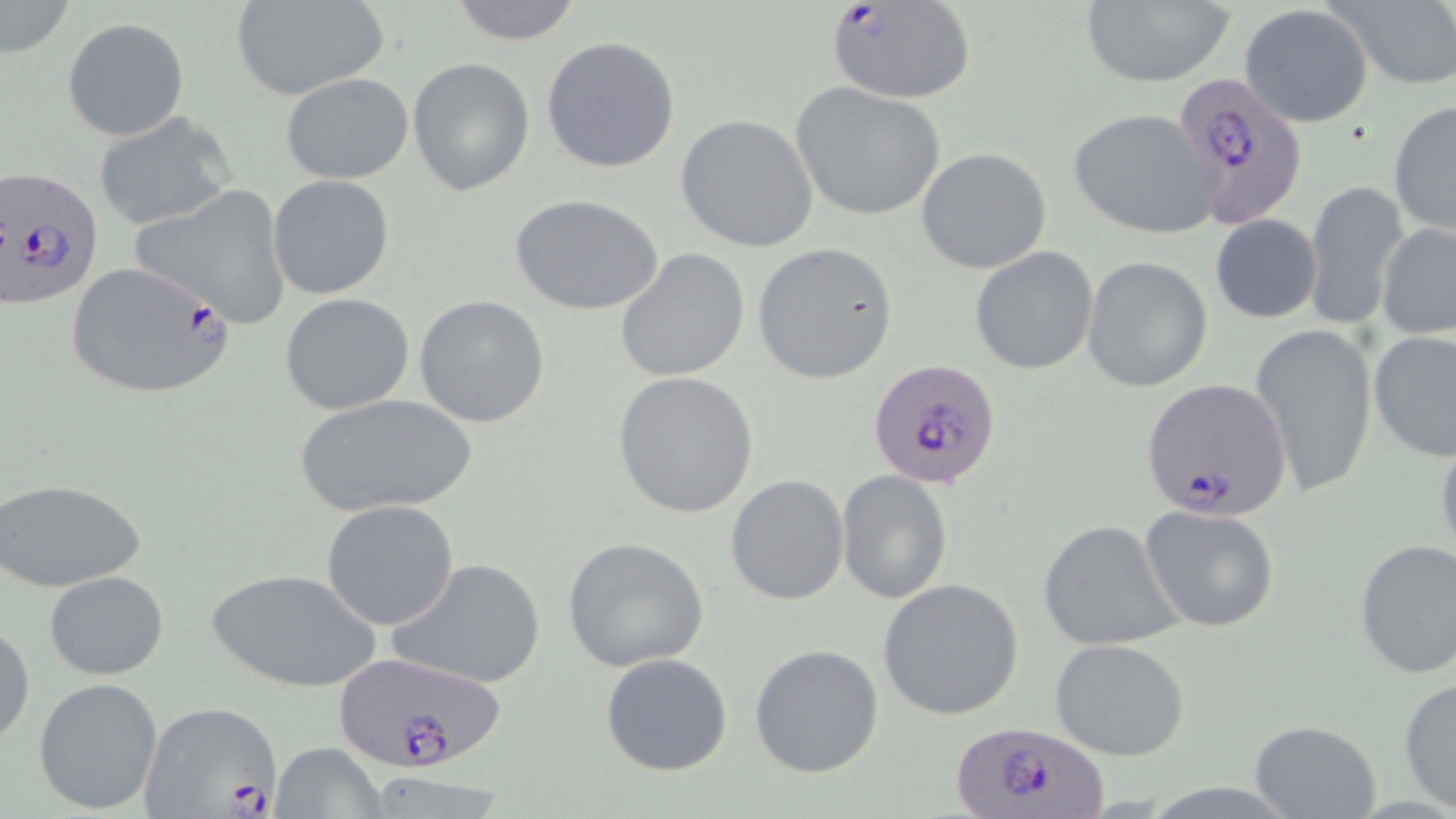

slide-level diagnosis = Plasmodium falciparum
field of view = single
modality = optical microscopy
image size = 1456×819 pixels
Plasmodium falciparum-infected red blood cell locations = approximate bounding boxes as (x1,y1)-(x2,y2) corner pairs in pixels: (826,1)-(975,104), (1171,71)-(1308,229), (1,165)-(105,309), (63,261)-(235,401), (868,358)-(1001,490), (1140,378)-(1292,519), (330,650)-(509,777), (141,700)-(286,818), (948,718)-(1111,819)
preparation = thin blood smear
stain = May-Grünwald-Giemsa
uninfected red blood cell locations = approximate bounding boxes as (x1,y1)-(x2,y2) corner pairs in pixels: (447,0)-(584,45), (1079,0)-(1236,88), (234,1)-(389,101), (1331,1)-(1456,91), (2,2)-(74,59), (1238,5)-(1374,128), (62,18)-(189,141), (541,36)-(681,174), (407,58)-(534,195), (281,73)-(414,184), (789,81)-(947,222), (1388,99)-(1455,238), (1068,109)-(1218,239), (95,112)-(238,233), (675,113)-(819,253), (917,147)-(1051,275), (267,175)-(396,300), (1304,178)-(1409,333), (130,183)-(294,329), (511,194)-(665,317), (1208,215)-(1322,324), (1377,220)-(1456,341), (752,243)-(898,385), (970,245)-(1098,376), (614,248)-(750,381), (1082,256)-(1213,394), (280,292)-(415,416), (414,295)-(551,428), (1250,321)-(1378,500), (1368,330)-(1456,461), (611,369)-(761,518), (291,393)-(478,520), (1434,430)-(1456,566), (836,471)-(954,605), (725,474)-(850,607), (1,478)-(146,591), (321,499)-(459,630), (1139,506)-(1280,631), (1037,519)-(1186,651), (561,536)-(709,671), (1353,538)-(1456,679), (386,557)-(546,690), (207,566)-(381,693), (44,570)-(168,679), (876,578)-(1026,720), (0,621)-(35,750), (1049,637)-(1191,760), (750,643)-(884,778), (601,652)-(733,775), (33,677)-(163,814), (1397,677)-(1456,814), (1248,719)-(1384,818), (270,741)-(389,818)
magnification = 1000x